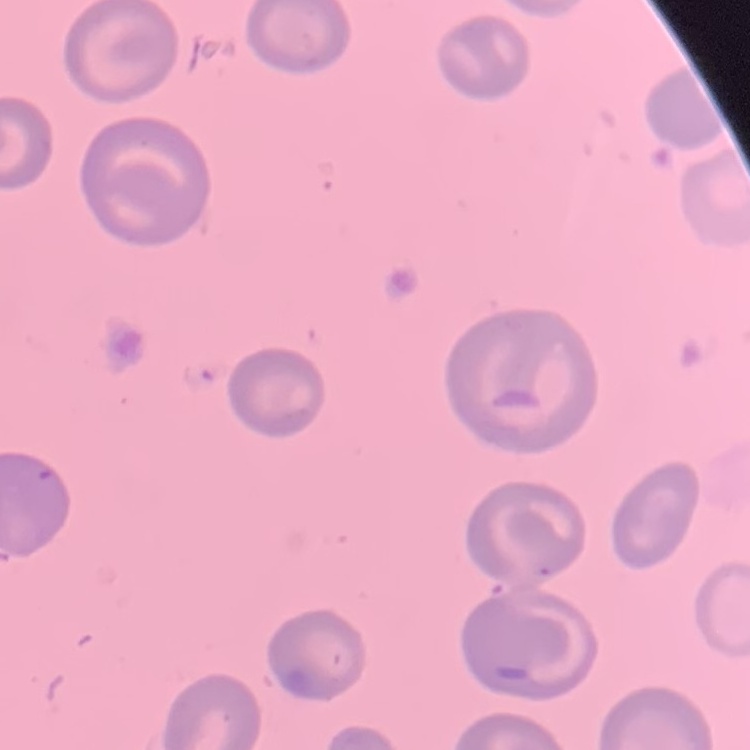
{
  "red_blood_cell_morphology": "no rouleaux formation",
  "image_type": "square crop of a larger photomicrograph",
  "preparation": "thin blood film",
  "stain": "Field's or Giemsa"
}